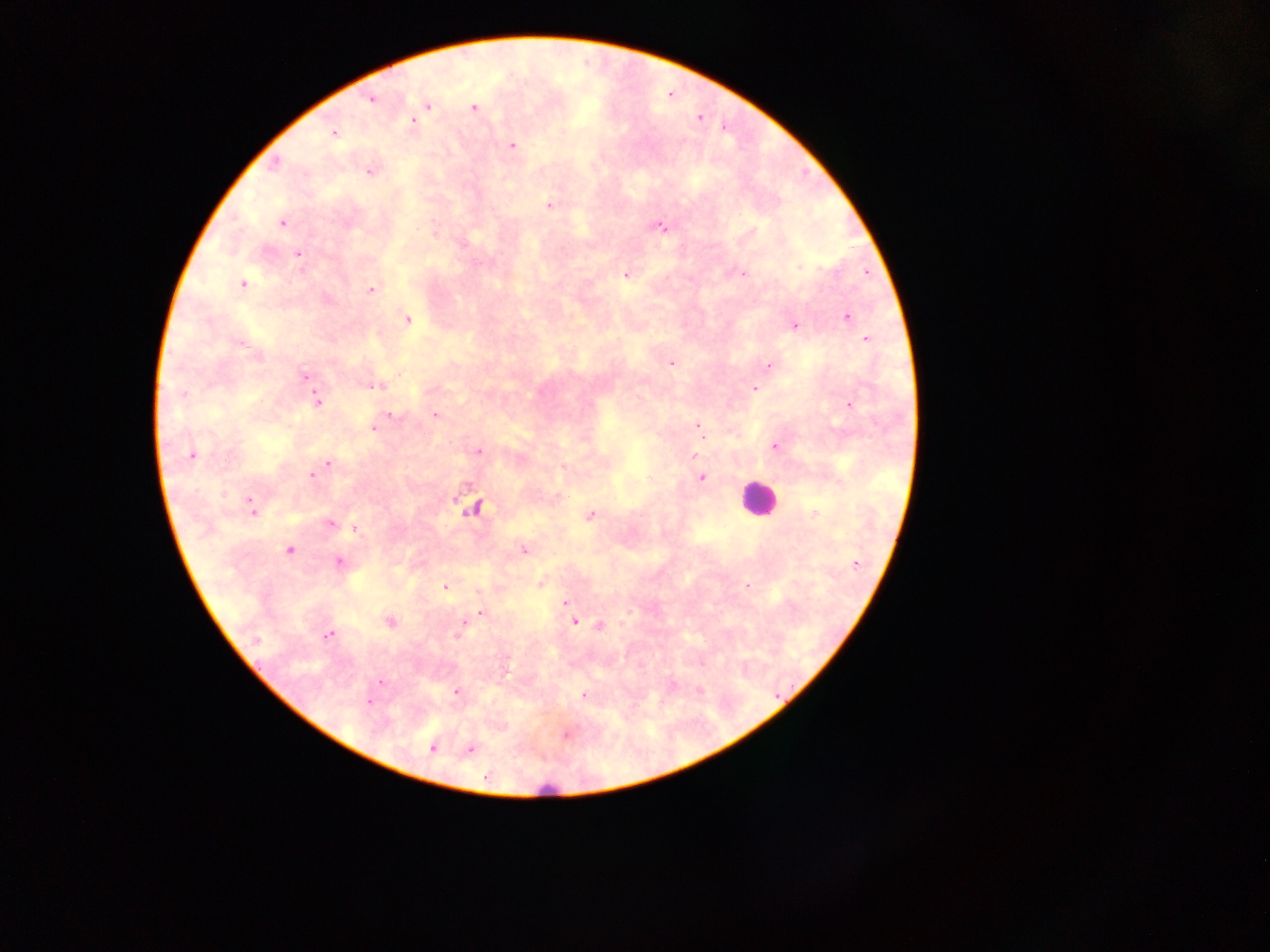 Approximate centers as x y in pixels. Plasmodium parasite locations: 370 100; 428 105; 474 108; 414 121; 334 134; 512 145; 275 164; 369 173; 549 205; 283 223; 661 227; 299 254; 799 267; 743 273; 866 273; 625 275; 243 284; 371 290; 847 317; 407 320; 795 326; 866 340; 671 363; 769 366; 305 376; 374 386; 754 389; 183 396; 319 403; 849 404; 391 415; 435 415; 698 427; 374 428; 775 446; 478 452; 192 455; 695 455; 328 464; 324 468; 312 475; 702 478; 252 504; 471 508; 813 514; 590 515; 330 523; 354 528; 289 550; 524 550; 339 562; 856 563; 746 585; 445 587; 566 603; 479 612; 389 622; 574 622; 600 626; 328 635; 457 635; 256 640; 380 681; 457 691; 584 695; 369 702; 431 748; 471 749. Leukocyte locations: 757 499. Thick blood film. Photographed through a microscope with a mobile-phone camera. Sample from Ghana. Image is 1270×952 pixels. Single field of view.